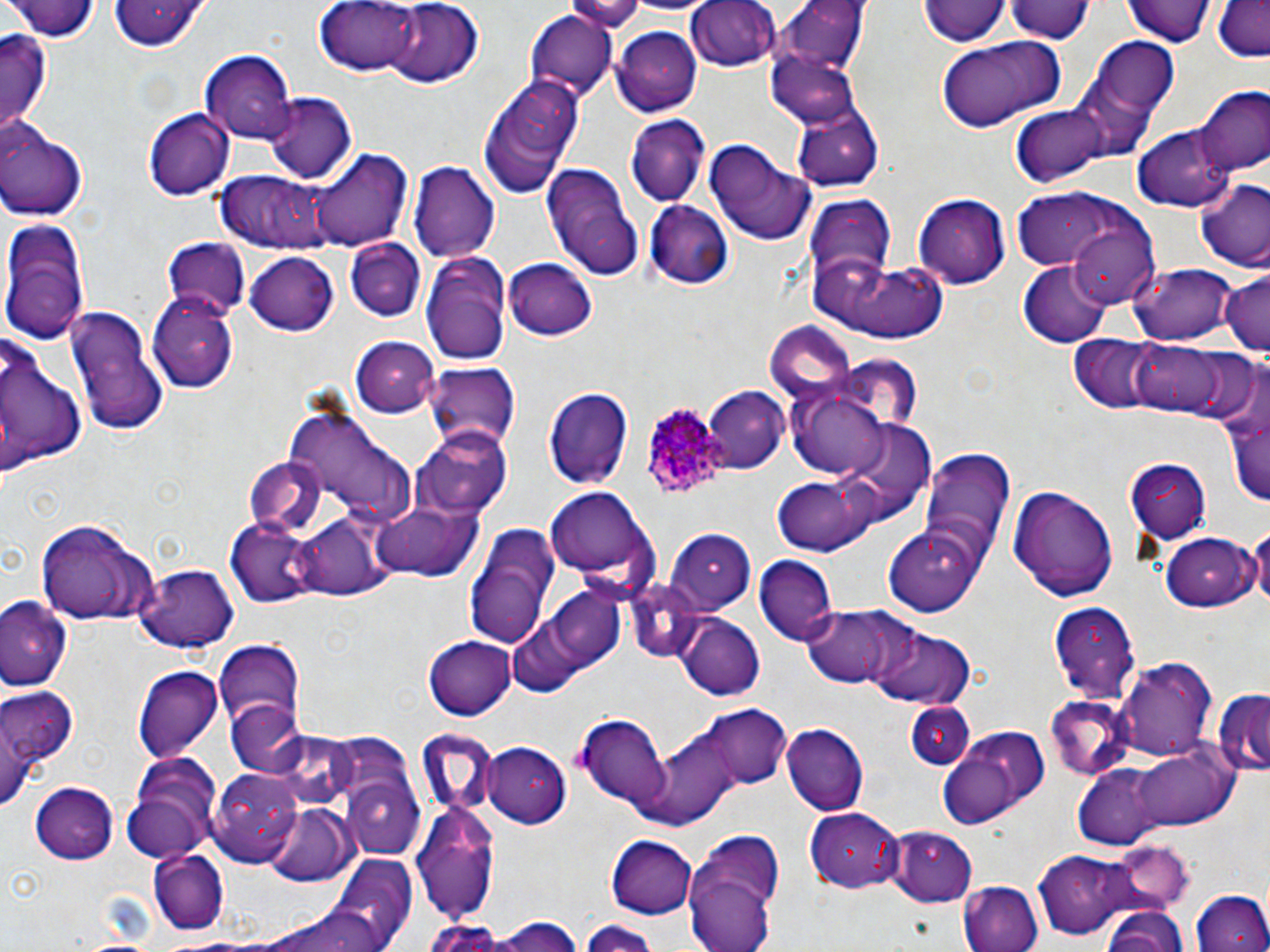

{
  "slide_level_diagnosis": "Plasmodium ovale",
  "uninfected_red_blood_cell_locations": "approximate bounding boxes as (x1, y1, x2, y2) in pixels: (10, 0, 100, 43), (108, 0, 210, 51), (317, 0, 422, 73), (564, 0, 644, 28), (686, 0, 782, 72), (922, 0, 1007, 49), (1125, 0, 1216, 47), (1002, 1, 1096, 44), (383, 2, 483, 88), (773, 2, 866, 79), (1210, 2, 1270, 60), (526, 11, 618, 101), (612, 27, 701, 114), (1, 29, 52, 130), (935, 35, 1066, 133), (1089, 36, 1178, 125), (199, 49, 296, 143), (771, 49, 861, 127), (480, 75, 584, 197), (1195, 88, 1269, 176), (264, 93, 356, 184), (1007, 101, 1116, 189), (791, 105, 884, 190), (143, 107, 234, 199), (625, 114, 711, 209), (0, 120, 88, 221), (1135, 125, 1232, 211), (704, 138, 817, 248), (311, 149, 408, 252), (409, 162, 498, 265), (542, 164, 643, 281), (219, 171, 332, 250), (1194, 179, 1270, 274), (1011, 188, 1153, 280), (913, 191, 1010, 287), (803, 195, 895, 286), (645, 199, 734, 289), (1066, 218, 1161, 305), (1, 221, 89, 340), (346, 238, 426, 320), (161, 240, 253, 318), (422, 251, 512, 363), (245, 253, 341, 336), (815, 258, 949, 342), (504, 259, 596, 340), (1018, 262, 1113, 346), (1130, 263, 1234, 346), (1218, 273, 1270, 356), (147, 289, 242, 392), (66, 304, 166, 438), (765, 322, 857, 401), (0, 326, 90, 484), (1070, 335, 1168, 411), (350, 337, 440, 415), (1127, 339, 1230, 415), (423, 361, 518, 449), (792, 384, 891, 478), (547, 386, 633, 489), (701, 388, 789, 474), (1223, 392, 1270, 513), (282, 405, 414, 525), (417, 425, 514, 516), (918, 446, 1017, 567), (244, 458, 326, 538), (1125, 460, 1211, 544), (772, 475, 882, 557), (1008, 483, 1119, 602), (547, 488, 652, 578), (371, 500, 484, 583), (295, 510, 390, 599), (36, 516, 160, 624), (1249, 519, 1270, 617), (228, 520, 320, 608), (460, 522, 564, 651), (884, 525, 985, 616), (666, 526, 754, 608), (1158, 532, 1262, 612), (754, 555, 836, 647), (139, 563, 239, 650), (627, 576, 713, 660), (540, 586, 628, 670), (0, 598, 69, 691), (1048, 605, 1139, 702), (801, 606, 906, 690), (505, 612, 597, 699), (676, 612, 766, 700), (857, 617, 974, 712), (425, 635, 516, 721), (214, 641, 306, 737), (1118, 656, 1218, 763), (135, 665, 224, 760), (0, 682, 77, 796), (1214, 689, 1270, 777), (1043, 697, 1135, 783), (228, 703, 311, 780), (907, 704, 974, 770), (695, 707, 792, 791), (574, 714, 674, 809), (783, 723, 869, 814), (634, 729, 745, 827), (417, 730, 506, 812), (936, 734, 1036, 829), (482, 740, 574, 828), (1126, 744, 1237, 833), (121, 757, 222, 861), (1067, 760, 1193, 849), (208, 767, 306, 865), (345, 773, 424, 858), (30, 780, 118, 863), (264, 803, 359, 885), (412, 805, 500, 923), (806, 806, 903, 890), (882, 824, 978, 905), (682, 830, 786, 952), (609, 834, 699, 919), (1106, 841, 1193, 914), (1035, 851, 1136, 939), (151, 852, 228, 934), (324, 855, 417, 952), (961, 883, 1043, 952), (1191, 891, 1270, 952), (268, 904, 391, 952), (1100, 905, 1190, 952), (490, 916, 585, 952), (581, 920, 662, 951), (421, 921, 508, 952)",
  "image_size": "1270×952 pixels",
  "modality": "light microscopy",
  "magnification": "1000x",
  "plasmodium_ovale_infected_red_blood_cell_locations": "approximate bounding boxes as (x1, y1, x2, y2) in pixels: (640, 398, 737, 504)",
  "stain": "May-Grünwald-Giemsa",
  "preparation": "thin blood film",
  "field_of_view": "one of a larger specimen"
}